Give the position of every leukocyte visible.
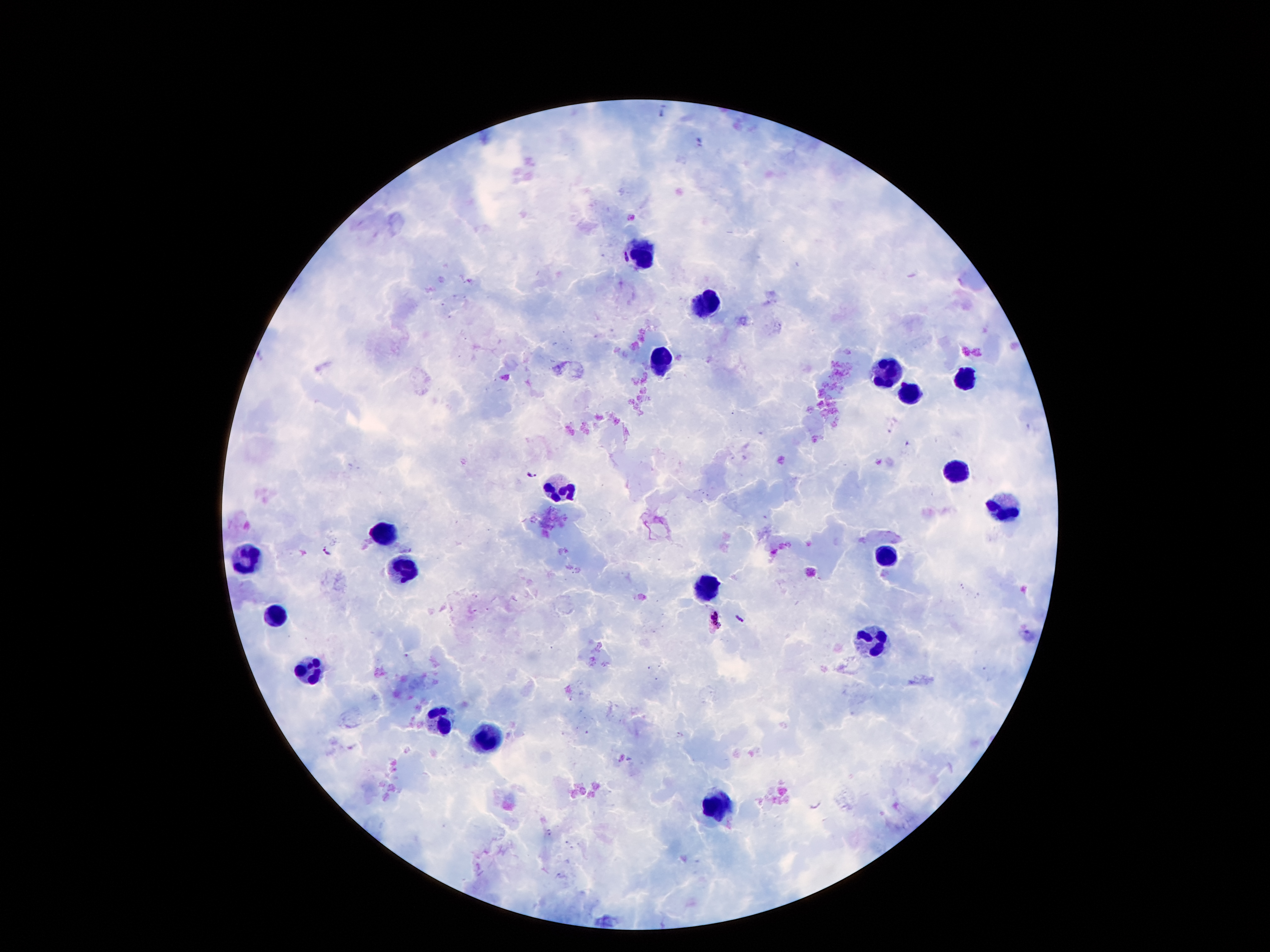
Approximate centers as {x, y} in pixels.
Leukocytes: {642, 254}, {706, 303}, {659, 364}, {889, 371}, {967, 378}, {907, 396}, {953, 469}, {563, 491}, {1009, 508}, {387, 533}, {246, 557}, {889, 559}, {407, 567}, {706, 587}, {276, 612}, {869, 638}, {306, 666}, {437, 718}, {486, 738}, {718, 806}.

Plasmodium parasite locations = {661, 112}, {531, 474}, {327, 551}, {739, 620}, {716, 621}
patient malaria status = positive for Plasmodium falciparum
stain = Giemsa
capture = smartphone camera through the microscope eyepiece
preparation = thick blood smear
field of view = single
image size = 1270×952 pixels
magnification = 100x